Describe the morphology of the erythrocytes.
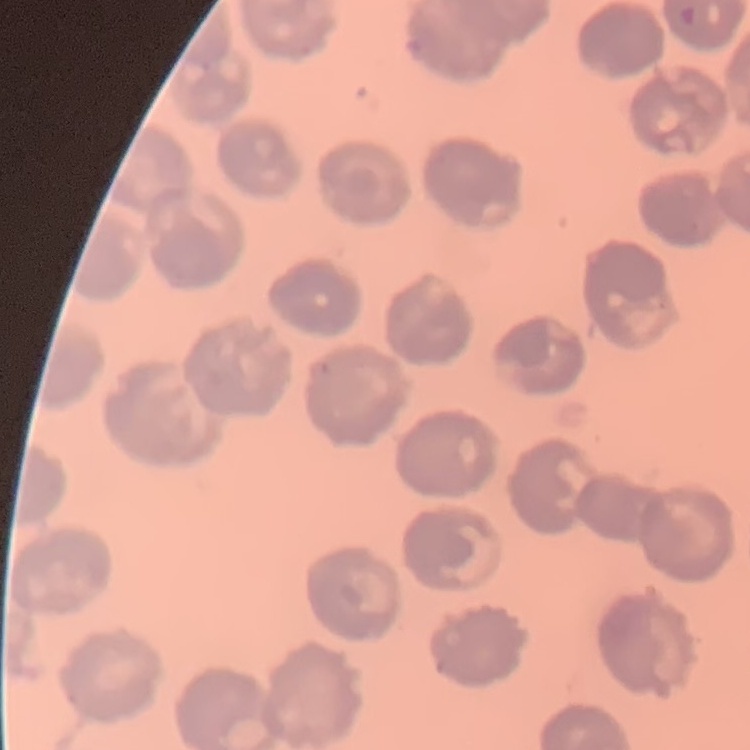

No rouleaux formation.

{
  "image_type": "square crop of a larger photomicrograph",
  "stain": "Field's or Giemsa",
  "preparation": "thin blood smear"
}